Locate every blood parasite and identify its species.
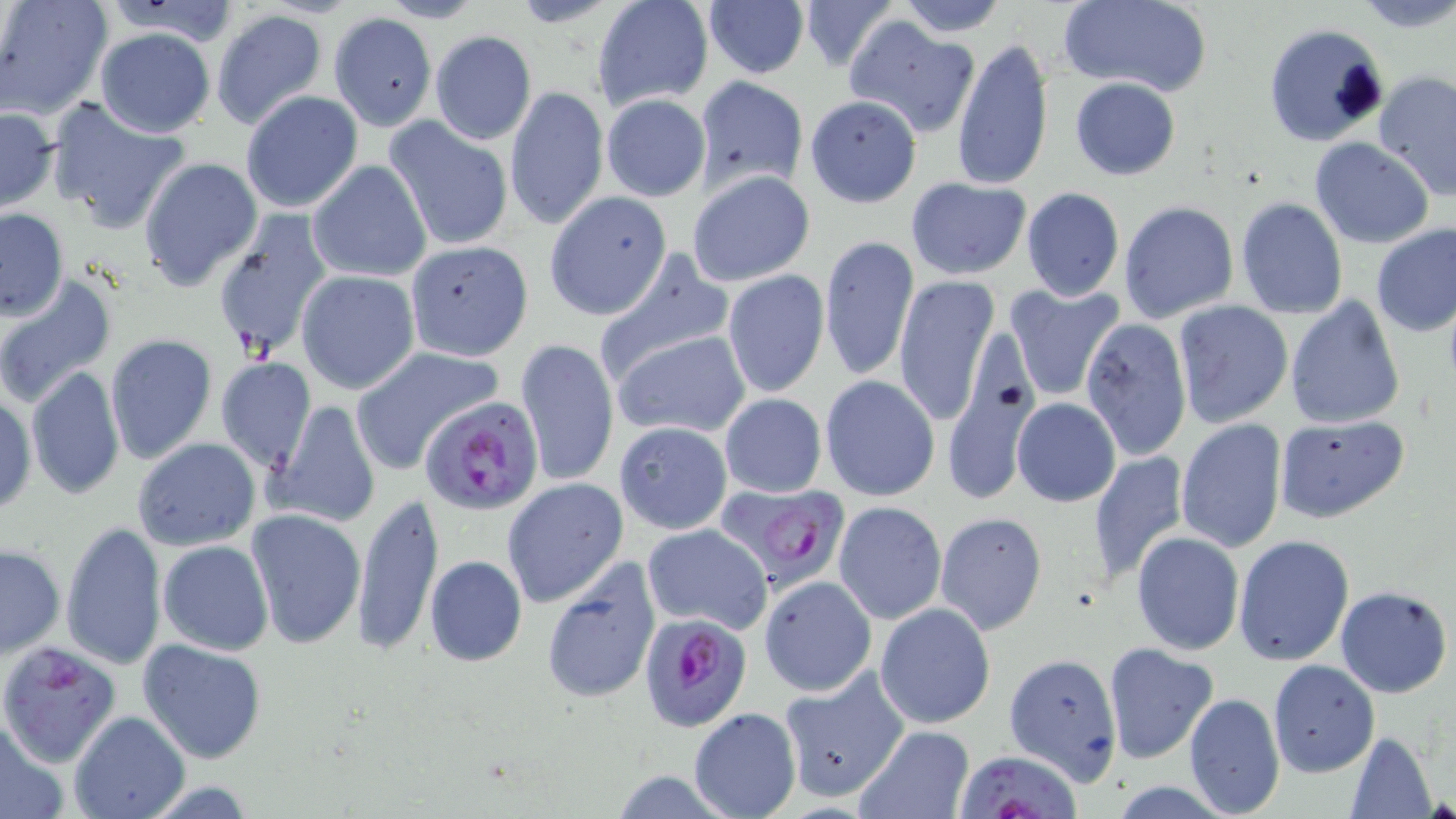
Approximate bounding boxes as (x1, y1, x2, y2) in pixels.
Plasmodium falciparum-infected red blood cells: (420, 395, 544, 516), (719, 481, 850, 594), (639, 612, 752, 732), (2, 641, 120, 774), (949, 747, 1086, 819).
No Plasmodium ovale, Plasmodium malariae, Plasmodium vivax, Babesia divergens, or Trypanosoma brucei observed.

slide-level diagnosis = Plasmodium falciparum
image size = 1456×819 pixels
modality = optical microscopy
preparation = thin blood smear
magnification = 1000x
stain = May-Grünwald-Giemsa
uninfected red blood cell locations = approximate bounding boxes as (x1, y1, x2, y2) in pixels: (1, 0, 111, 120), (591, 0, 715, 110), (895, 0, 1011, 37), (1058, 0, 1212, 96), (1353, 0, 1456, 30), (372, 1, 486, 24), (796, 1, 900, 74), (703, 3, 810, 79), (210, 8, 330, 131), (329, 12, 438, 131), (845, 19, 980, 137), (1262, 22, 1388, 146), (93, 27, 217, 138), (430, 31, 537, 144), (952, 36, 1054, 192), (1373, 70, 1456, 201), (694, 75, 809, 191), (1068, 77, 1180, 180), (505, 86, 608, 229), (240, 90, 363, 213), (601, 93, 710, 201), (804, 94, 923, 207), (44, 95, 191, 234), (0, 106, 59, 212), (384, 116, 514, 252), (1309, 136, 1435, 248), (139, 157, 263, 291), (307, 160, 432, 283), (687, 170, 815, 286), (904, 177, 1032, 280), (1020, 186, 1124, 303), (545, 192, 672, 320), (1234, 198, 1348, 320), (1118, 201, 1238, 323), (0, 207, 69, 320), (212, 210, 335, 363), (1370, 223, 1456, 337), (819, 233, 919, 381), (404, 240, 533, 360), (593, 250, 732, 379), (295, 270, 420, 393), (722, 270, 830, 398), (893, 273, 1001, 425), (0, 275, 116, 407), (1003, 282, 1126, 400), (1284, 295, 1405, 431), (1171, 301, 1293, 430), (1080, 317, 1193, 462), (611, 329, 751, 440), (105, 334, 216, 466), (515, 337, 619, 487), (349, 345, 503, 474), (937, 350, 1056, 502), (215, 357, 315, 470), (24, 365, 124, 501), (821, 375, 940, 501), (1, 392, 36, 518), (720, 392, 826, 498), (1012, 398, 1121, 506), (266, 399, 382, 530), (1276, 414, 1408, 524), (1175, 418, 1288, 554), (614, 421, 733, 534), (131, 438, 261, 553), (1087, 450, 1189, 584), (502, 478, 630, 609), (352, 490, 445, 657), (833, 500, 946, 625), (935, 510, 1047, 635), (245, 511, 365, 652), (60, 520, 167, 672), (642, 523, 772, 634), (1131, 531, 1245, 656), (1233, 535, 1356, 667), (157, 540, 273, 655), (1, 543, 65, 658), (423, 555, 527, 667), (540, 558, 659, 704), (758, 575, 877, 696), (1335, 587, 1452, 697), (875, 603, 995, 728), (138, 637, 267, 763), (1104, 642, 1219, 764), (1003, 652, 1124, 783), (1267, 660, 1379, 776), (777, 668, 908, 802), (1181, 678, 1369, 800), (1183, 692, 1285, 817), (688, 708, 799, 819), (70, 710, 190, 819), (0, 712, 67, 819), (854, 727, 976, 819), (1342, 731, 1438, 818)
field of view = single